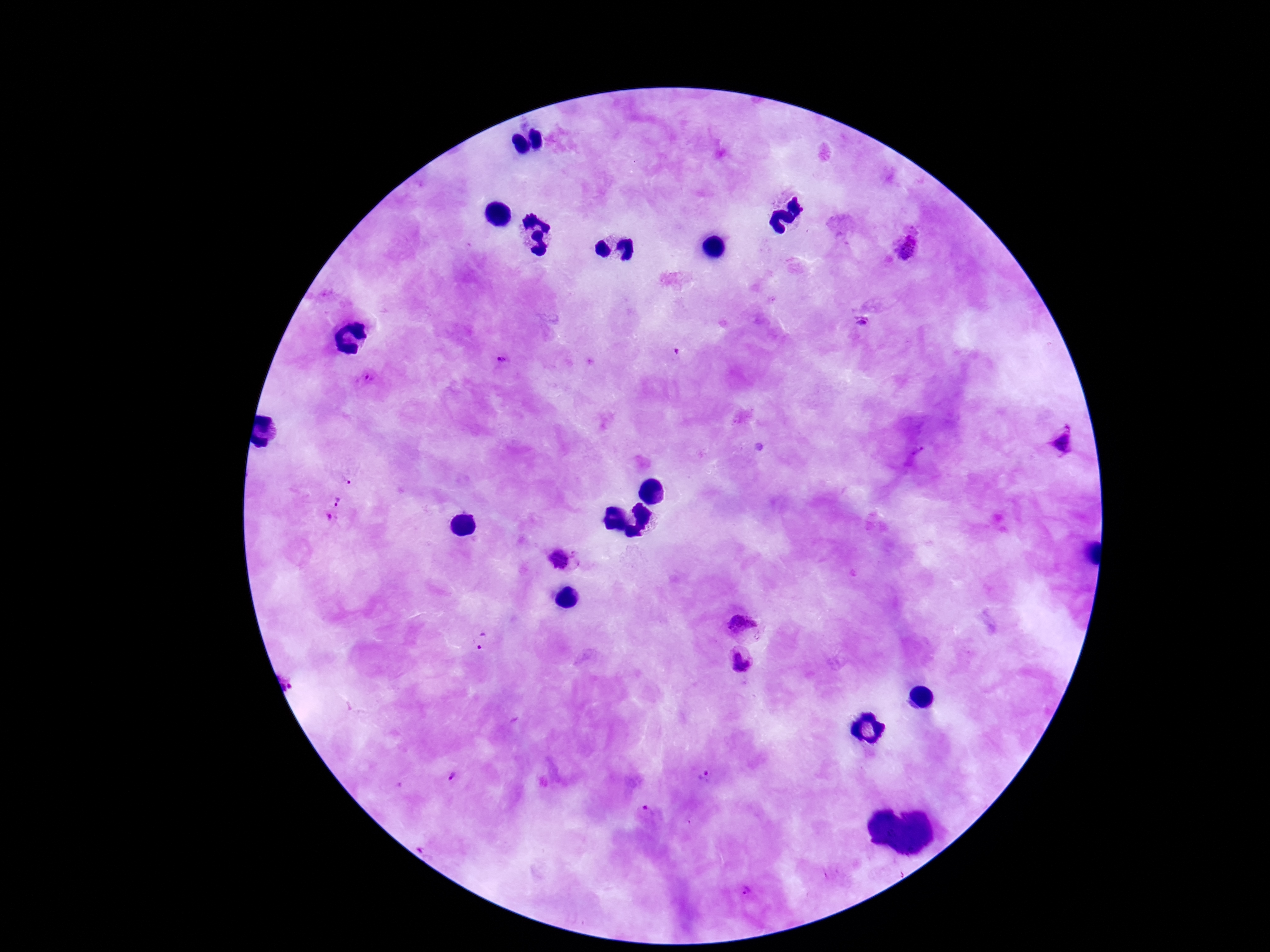
Approximate centers as {x, y} in pixels. Plasmodium parasite locations: {907, 248}, {862, 322}, {499, 359}, {362, 380}, {1063, 443}, {332, 509}, {564, 560}, {747, 619}, {482, 644}, {737, 664}, {453, 778}, {704, 779}, {646, 812}, {748, 889}. Image is 1270×952 pixels. Patient malaria status: positive. One field from this slide. 100x magnification. Thick blood film. Giemsa stain. Smartphone photograph taken through the microscope eyepiece.